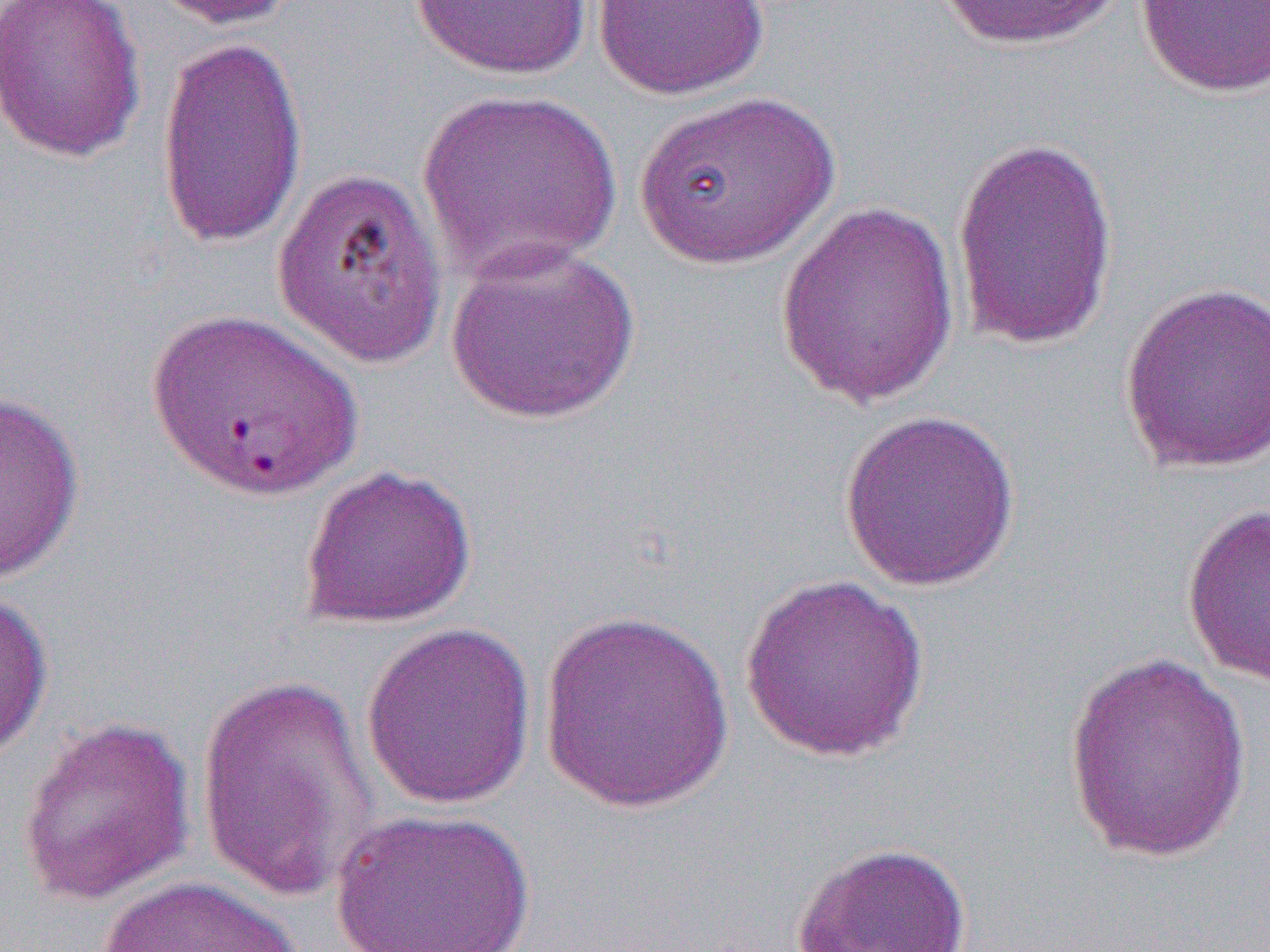
slide-level diagnosis = Plasmodium falciparum
image size = 1270×952 pixels
modality = light microscopy
field of view = single
uninfected red blood cell locations = approximate bounding boxes as [x1, y1, x2, y2] in pixels: [0, 0, 148, 164], [146, 0, 311, 31], [410, 0, 593, 80], [931, 0, 1127, 51], [590, 1, 770, 100], [1134, 1, 1269, 98], [155, 34, 309, 252], [415, 87, 625, 281], [632, 89, 841, 270], [949, 132, 1120, 353], [271, 163, 449, 369], [773, 200, 961, 408], [444, 239, 643, 425], [1119, 279, 1270, 475], [143, 306, 363, 502], [0, 390, 85, 583], [839, 409, 1021, 592], [298, 463, 476, 630], [1182, 501, 1270, 689], [739, 574, 930, 762], [0, 583, 54, 764], [537, 607, 737, 813], [361, 620, 537, 810], [1062, 649, 1254, 864], [194, 671, 381, 903], [16, 714, 196, 906], [329, 807, 538, 952], [791, 841, 973, 952], [95, 875, 302, 952]
preparation = thin blood smear
magnification = 1000x